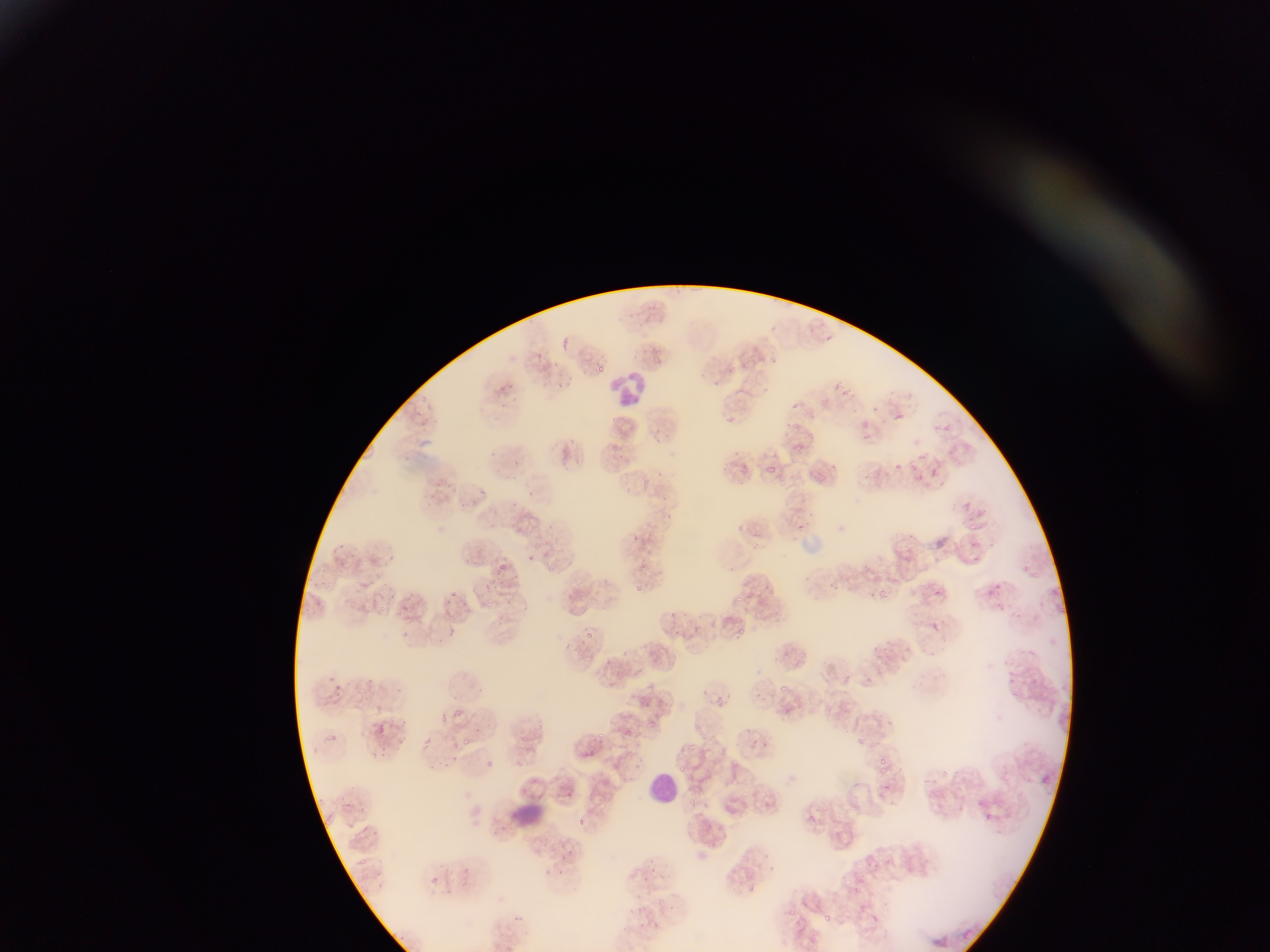

Approximate bounding boxes as left top right bottom in pixels. Leukocyte locations: 612 369 674 407; 647 766 677 802; 513 802 549 833. Malaria parasite locations: 560 337 568 352; 793 401 801 409; 427 404 434 412; 794 421 802 430; 798 442 806 450; 895 463 903 469; 767 466 777 472; 478 489 487 496; 662 494 669 503; 666 511 673 519; 633 534 641 539; 530 539 546 549; 638 540 647 547; 528 553 540 562; 896 561 905 566; 498 562 504 571; 543 562 552 567; 632 583 641 591; 451 590 459 597; 878 590 888 599; 934 590 944 596; 737 596 745 603; 487 597 494 608; 403 607 411 611; 445 611 454 614; 685 618 695 624; 447 627 457 636; 584 632 595 638; 867 677 875 684; 779 686 787 692; 830 692 840 700; 718 696 724 707; 440 715 447 725; 379 727 388 731; 746 727 755 735; 625 729 633 735; 465 733 474 745; 690 744 698 750; 678 747 686 753; 879 756 888 766; 882 765 887 774; 566 776 574 784; 883 783 889 791; 567 790 573 798; 689 799 698 805; 809 813 818 822; 743 852 754 862; 649 868 658 873; 541 869 552 875; 784 910 796 917; 825 916 833 923 | approximate x y pixel centers of objects too small to bound: 829 338; 539 356; 752 360; 601 369; 836 389; 810 433; 578 462; 658 473; 533 493; 801 526; 649 536; 1036 575; 372 581; 999 586; 592 598; 449 601; 762 603; 382 609; 673 614; 452 617; 762 619; 742 631; 645 646; 583 653; 626 654; 802 656; 629 661; 379 708; 788 710; 652 724; 540 727; 636 733; 699 733; 601 735; 860 740; 403 742; 601 742; 631 758; 684 768; 989 816; 580 821; 364 861; 466 871. Image is 1270×952 pixels. Thin blood smear. Photographed through a microscope with a mobile-phone camera. Single field of view. Sample from Ghana.